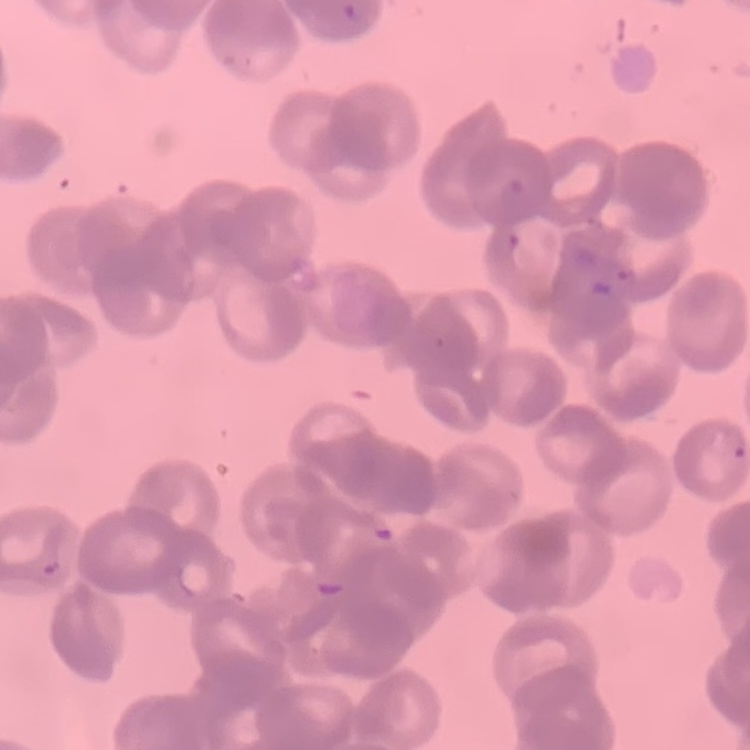
Summary:
  - Red blood cell morphology: rouleaux formation
  - Stain: Field's or Giemsa
  - Preparation: thin blood film
  - Image type: square crop of a larger photomicrograph